Locate every uninfected red blood cell.
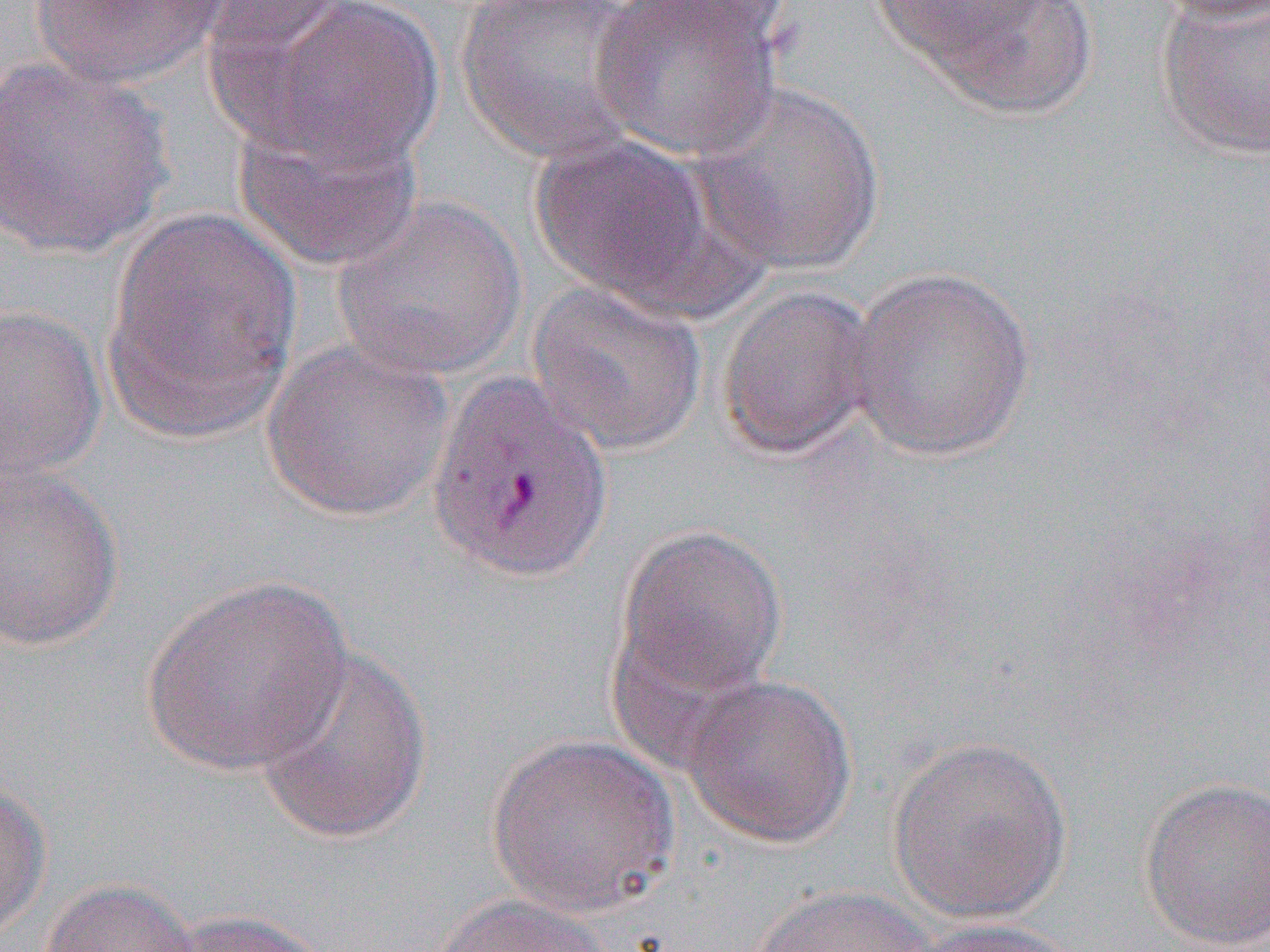
Approximate bounding boxes as named x1/y1/x2/y2 corners in pixels.
Uninfected red blood cells: (x1=29, y1=0, x2=228, y2=89), (x1=230, y1=0, x2=446, y2=172), (x1=455, y1=0, x2=652, y2=166), (x1=591, y1=0, x2=784, y2=164), (x1=867, y1=0, x2=1100, y2=119), (x1=1149, y1=0, x2=1270, y2=26), (x1=192, y1=1, x2=359, y2=67), (x1=1155, y1=2, x2=1270, y2=162), (x1=0, y1=54, x2=175, y2=260), (x1=688, y1=80, x2=887, y2=277), (x1=231, y1=105, x2=426, y2=274), (x1=527, y1=131, x2=738, y2=312), (x1=332, y1=193, x2=528, y2=381), (x1=102, y1=206, x2=303, y2=440), (x1=843, y1=267, x2=1036, y2=462), (x1=527, y1=280, x2=708, y2=457), (x1=715, y1=283, x2=880, y2=462), (x1=0, y1=302, x2=106, y2=484), (x1=261, y1=339, x2=454, y2=522), (x1=0, y1=462, x2=125, y2=651), (x1=614, y1=524, x2=789, y2=703), (x1=139, y1=575, x2=353, y2=776), (x1=252, y1=645, x2=434, y2=846), (x1=681, y1=674, x2=858, y2=848), (x1=888, y1=733, x2=1073, y2=925), (x1=485, y1=734, x2=681, y2=916), (x1=1137, y1=776, x2=1270, y2=951), (x1=0, y1=777, x2=51, y2=942), (x1=37, y1=878, x2=202, y2=952), (x1=751, y1=884, x2=941, y2=952), (x1=429, y1=894, x2=616, y2=952), (x1=158, y1=907, x2=336, y2=952), (x1=911, y1=917, x2=1087, y2=952).

Slide-level diagnosis: Plasmodium vivax. Thin blood smear. One field of a larger specimen. Optical microscopy. Captured at 1000x magnification. Image is 1270×952 pixels.